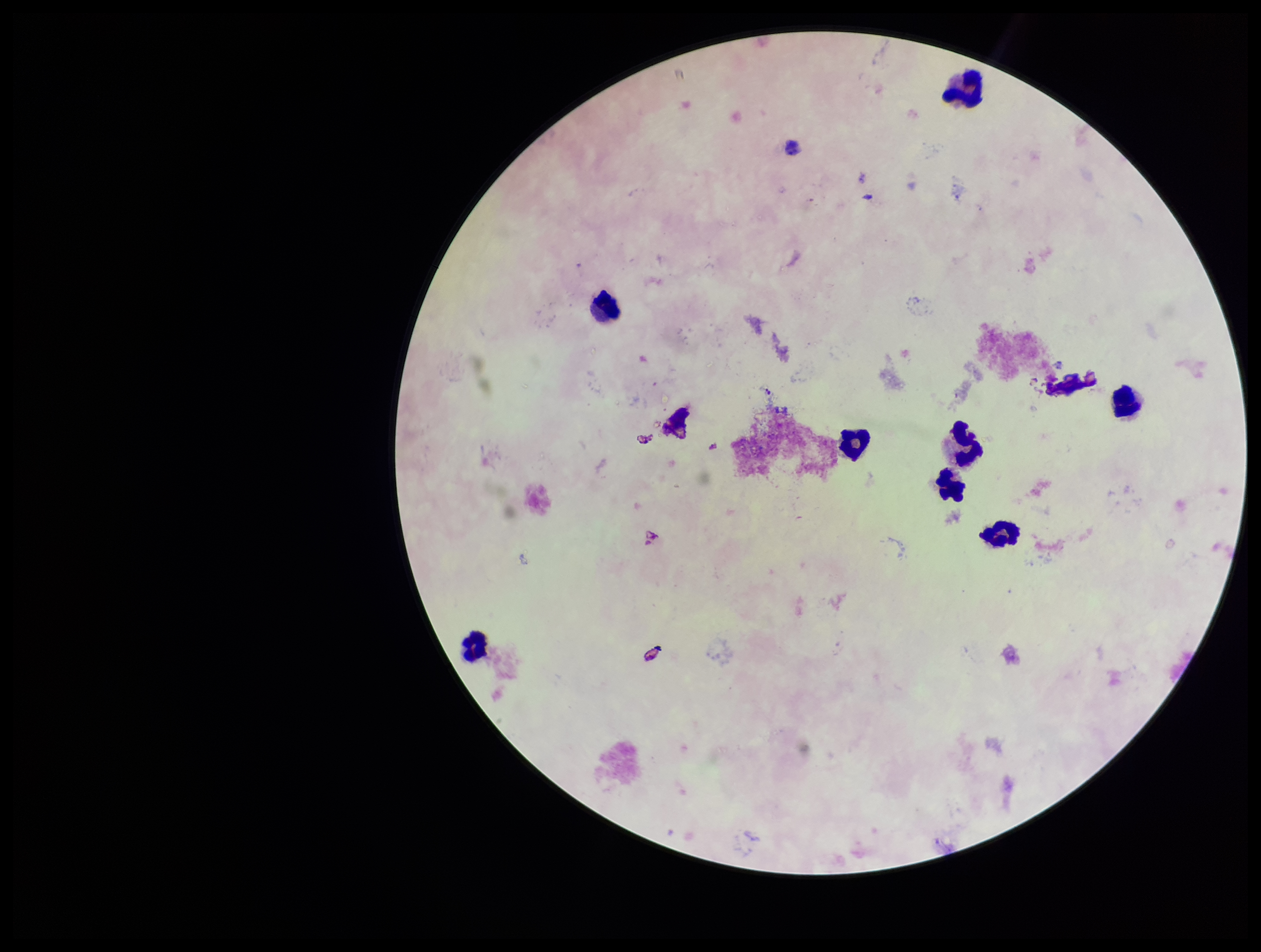

{
  "parasite_count": 0,
  "preparation": "thick smear",
  "capture": "smartphone photograph through the microscope eyepiece",
  "image_size": "1261×952 pixels",
  "leukocyte_count": 9,
  "stain": "Giemsa",
  "patient_malaria_status": "infected",
  "plasmodium_parasites": "none seen",
  "field_of_view": "single",
  "species_reported_for_this_patient": "Plasmodium falciparum"
}